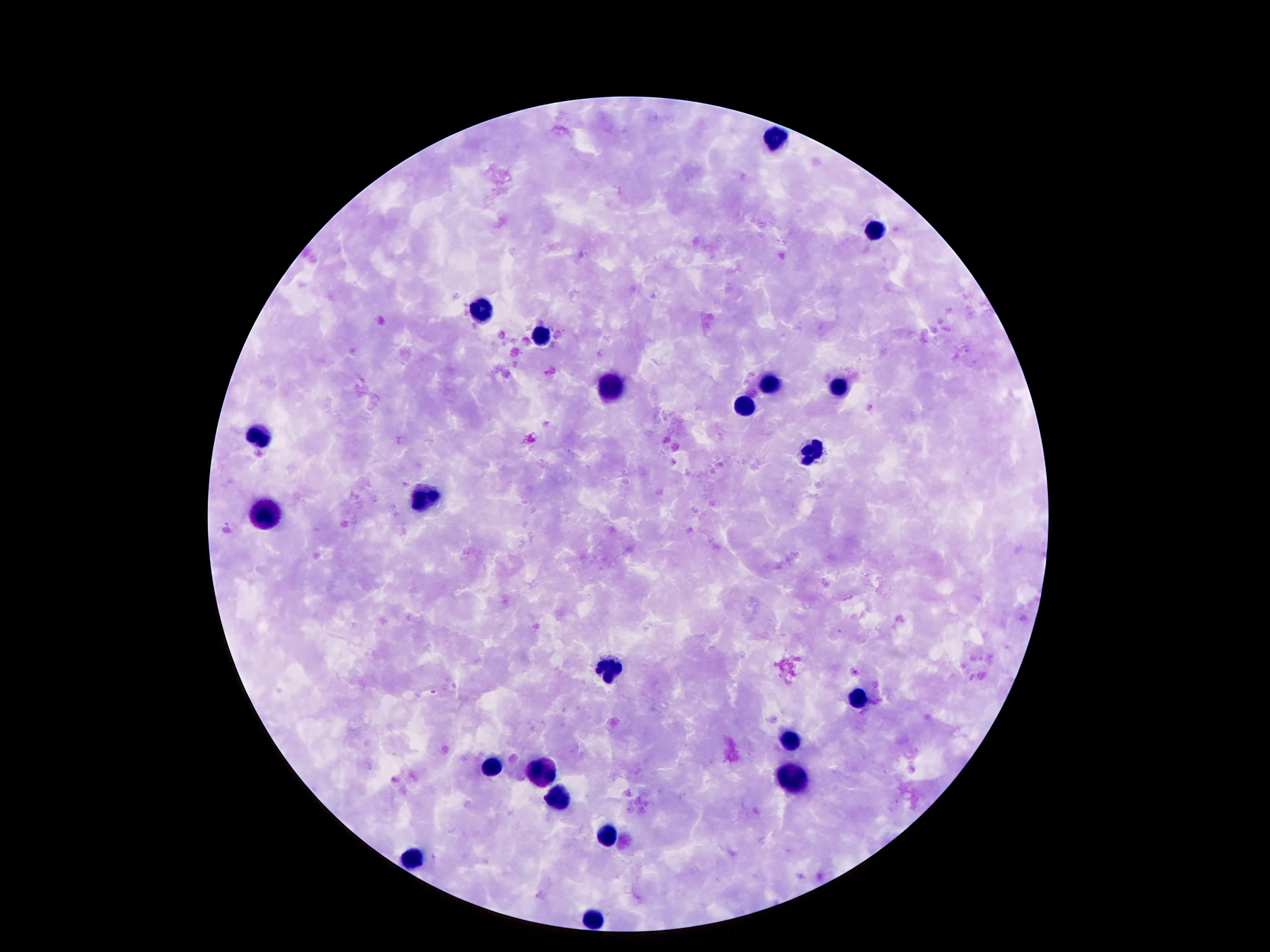

Approximate centers as [x, y] in pixels.
Summary:
  - Leukocyte locations: [772, 139], [874, 229], [481, 309], [538, 339], [767, 384], [838, 386], [611, 389], [745, 407], [259, 436], [810, 450], [424, 497], [266, 518], [599, 666], [863, 700], [792, 737], [486, 768], [540, 774], [792, 781], [556, 799], [608, 836], [413, 862], [595, 919]
  - Image size: 1270×952 pixels
  - Magnification: 100x
  - Preparation: thick blood film
  - Field of view: single
  - Stain: Giemsa
  - Patient malaria status: negative
  - Capture: smartphone camera through the microscope eyepiece